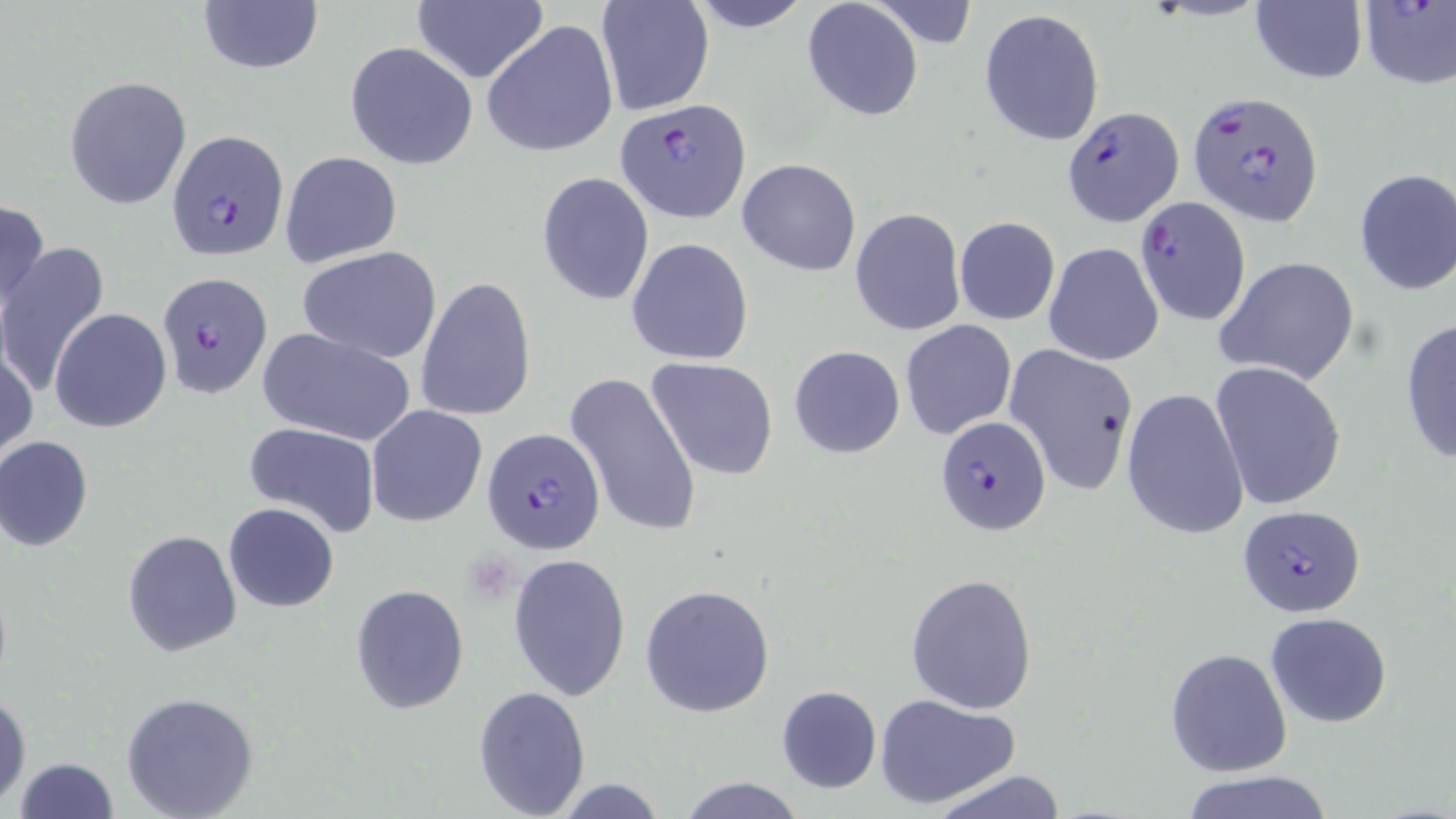 Approximate bounding boxes as [x1, y1, x2, y2] in pixels. Plasmodium falciparum-infected red blood cell locations: [1358, 0, 1456, 89], [1188, 91, 1325, 228], [616, 100, 750, 223], [1061, 106, 1182, 225], [166, 129, 290, 259], [1133, 196, 1252, 326], [137, 275, 273, 404], [936, 415, 1051, 536], [482, 427, 605, 557], [1237, 506, 1368, 615]. Uninfected red blood cell locations: [412, 0, 547, 86], [595, 0, 715, 117], [683, 0, 814, 31], [195, 1, 324, 77], [868, 1, 979, 50], [1250, 1, 1367, 85], [802, 2, 924, 120], [979, 9, 1105, 146], [483, 19, 618, 159], [344, 41, 478, 170], [64, 75, 193, 211], [278, 151, 402, 268], [737, 158, 862, 275], [1354, 168, 1456, 295], [536, 172, 654, 306], [0, 197, 49, 317], [850, 207, 965, 336], [953, 216, 1060, 325], [627, 238, 755, 365], [1042, 241, 1164, 366], [0, 242, 109, 396], [299, 245, 444, 363], [1214, 256, 1360, 386], [416, 276, 537, 422], [49, 308, 172, 433], [1398, 317, 1456, 466], [900, 320, 1017, 440], [255, 326, 417, 446], [1, 340, 37, 462], [1003, 343, 1139, 496], [789, 344, 906, 459], [647, 356, 779, 482], [1209, 362, 1348, 511], [564, 370, 703, 538], [1121, 388, 1251, 542], [367, 405, 488, 527], [245, 422, 382, 537], [0, 435, 94, 553], [223, 502, 339, 612], [122, 528, 242, 657], [507, 552, 632, 702], [904, 573, 1038, 714], [350, 584, 469, 714], [641, 584, 774, 718], [1265, 611, 1392, 728], [1165, 647, 1293, 776], [473, 686, 591, 817], [776, 686, 881, 794], [0, 690, 31, 809], [120, 690, 260, 818], [872, 691, 1021, 811], [13, 757, 120, 818], [927, 770, 1070, 819], [1178, 771, 1338, 819], [675, 776, 807, 818], [549, 778, 672, 817]. Slide-level diagnosis: Plasmodium falciparum. May-Grünwald-Giemsa stain. Single field of view. 1000x magnification. Optical microscopy. Thin blood film. Image is 1456×819 pixels.